Assess this cell for malaria.
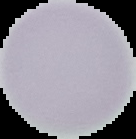
It is uninfected.

Summary:
  - Image size: 136×139 pixels
  - Image type: segmented cell region on a black background
  - Preparation: thin blood smear